Give the extent of all Plasmodium falciparum-infected red blood cells.
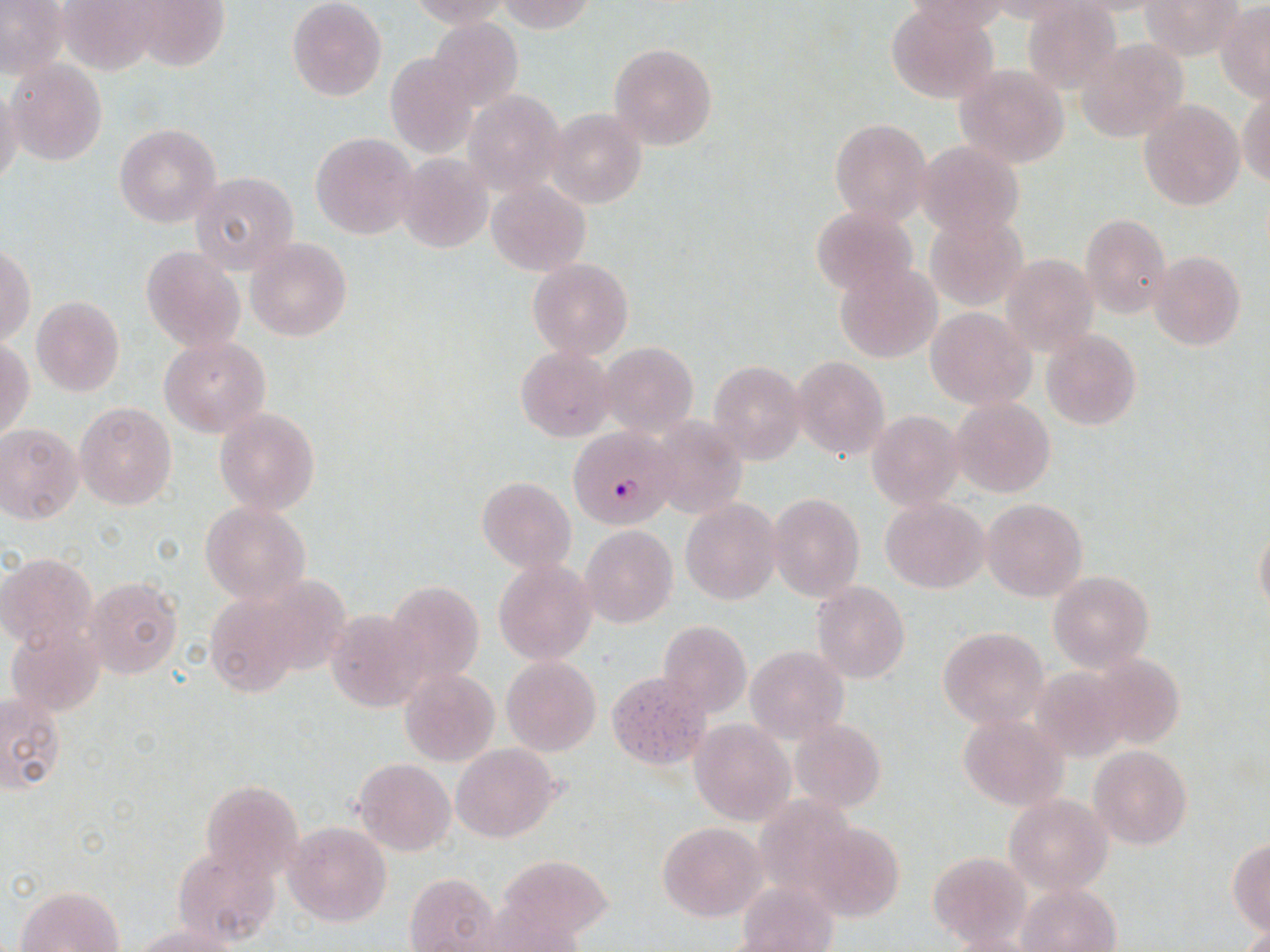

Approximate bounding boxes as (x1,y1)-(x2,y2) corner pairs in pixels.
Plasmodium falciparum-infected red blood cells: (569,428)-(675,527).

slide-level diagnosis = Plasmodium falciparum
field of view = one of a larger specimen
stain = May-Grünwald-Giemsa
magnification = 1000x
uninfected red blood cell locations = approximate bounding boxes as (x1,y1)-(x2,y2) corner pairs in pixels: (56,0)-(165,76), (117,0)-(230,73), (287,0)-(387,101), (406,0)-(513,29), (494,0)-(595,33), (903,1)-(1013,35), (1141,1)-(1243,60), (0,2)-(68,79), (1019,3)-(1120,91), (1217,3)-(1270,101), (884,5)-(1000,103), (428,17)-(522,108), (1076,40)-(1190,143), (609,43)-(718,151), (387,54)-(477,157), (6,58)-(108,167), (954,65)-(1070,168), (0,82)-(23,193), (1238,84)-(1270,188), (460,90)-(567,195), (1139,98)-(1246,211), (545,107)-(648,211), (828,117)-(931,224), (114,123)-(222,228), (311,132)-(420,241), (917,140)-(1025,240), (395,153)-(494,254), (190,172)-(300,276), (486,179)-(591,276), (812,206)-(915,295), (924,213)-(1027,310), (1080,213)-(1171,318), (245,237)-(352,342), (1,244)-(35,346), (142,246)-(246,353), (1149,250)-(1247,350), (1001,253)-(1099,357), (529,258)-(633,359), (835,263)-(942,363), (31,297)-(124,396), (925,307)-(1036,410), (1041,330)-(1141,429), (158,336)-(271,436), (1,338)-(36,441), (600,341)-(697,438), (516,346)-(615,441), (791,356)-(891,462), (708,361)-(806,463), (951,396)-(1055,497), (74,401)-(177,510), (215,407)-(320,515), (867,410)-(964,513), (652,416)-(747,521), (0,423)-(83,523), (478,477)-(576,573), (768,493)-(864,601), (882,497)-(987,593), (982,498)-(1087,603), (680,499)-(782,603), (200,500)-(312,604), (1254,521)-(1270,619), (580,526)-(677,628), (1,553)-(97,651), (494,559)-(596,665), (1049,571)-(1154,672), (85,576)-(183,678), (386,581)-(485,687), (812,581)-(909,684), (203,593)-(303,697), (324,610)-(428,711), (658,620)-(751,716), (6,621)-(105,717), (938,627)-(1049,729), (745,646)-(849,744), (1088,653)-(1189,752), (501,655)-(600,756), (1030,664)-(1132,762), (399,668)-(499,767), (607,670)-(709,769), (1,690)-(65,797), (957,715)-(1067,811), (790,718)-(886,814), (690,720)-(793,825), (452,743)-(565,842), (1089,745)-(1191,849), (355,757)-(456,855), (200,780)-(304,881), (1004,794)-(1112,894), (752,795)-(861,907), (806,819)-(905,923), (285,821)-(391,928), (657,821)-(765,921), (1229,841)-(1270,936), (174,848)-(278,949), (927,852)-(1027,945), (497,853)-(613,944), (405,872)-(501,950), (736,883)-(839,951), (1019,883)-(1120,951), (16,885)-(126,952), (133,921)-(248,951), (1239,924)-(1270,951)
image size = 1270×952 pixels
preparation = thin blood smear
modality = optical microscopy